Outline each uninfected red blood cell.
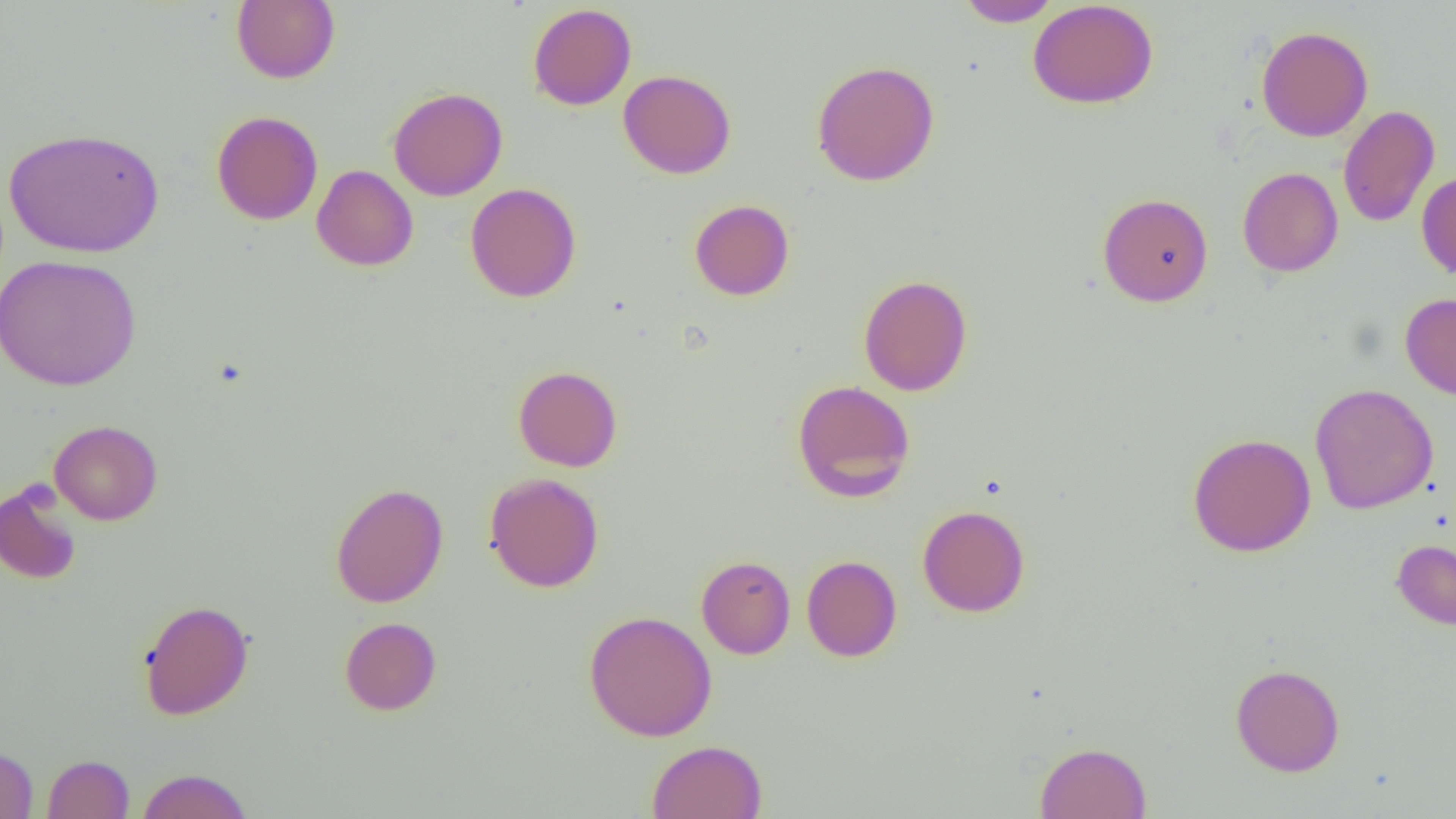
Approximate bounding boxes as (x1, y1, x2, y2) in pixels.
Uninfected red blood cells: (232, 0, 340, 84), (954, 0, 1062, 27), (1028, 0, 1159, 109), (527, 3, 636, 110), (1256, 26, 1372, 142), (812, 60, 940, 186), (618, 70, 736, 178), (388, 87, 508, 201), (1338, 105, 1440, 227), (212, 110, 323, 225), (4, 127, 164, 258), (312, 165, 418, 271), (1238, 167, 1343, 277), (1416, 170, 1456, 279), (466, 183, 582, 303), (1097, 192, 1213, 307), (689, 199, 794, 301), (0, 254, 142, 391), (858, 275, 972, 396), (1400, 293, 1456, 400), (513, 365, 622, 472), (792, 379, 915, 502), (1309, 383, 1438, 514), (49, 420, 163, 525), (1187, 433, 1317, 557), (484, 472, 604, 592), (0, 481, 82, 585), (330, 482, 448, 608), (917, 504, 1030, 617), (1391, 539, 1456, 630), (696, 555, 795, 659), (801, 555, 902, 662), (138, 599, 254, 721), (583, 610, 718, 742), (339, 617, 442, 715), (1230, 662, 1345, 777), (646, 740, 767, 819), (1035, 741, 1152, 819), (0, 746, 38, 818), (42, 754, 134, 818), (136, 768, 252, 819).

Slide-level diagnosis: no evidence of blood parasites. Thin blood film. Optical microscopy. 1000x magnification. Image is 1456×819 pixels. Single field of view.